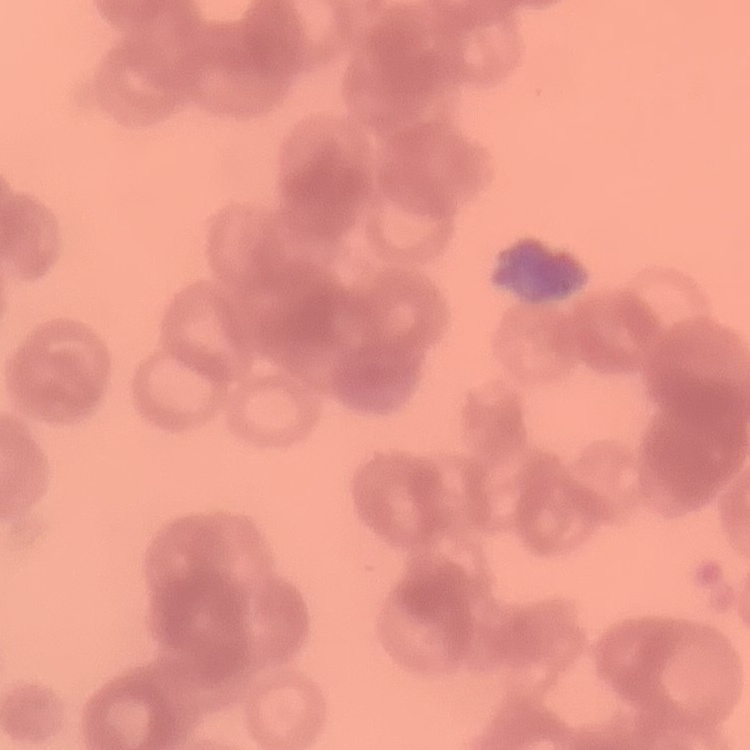
Summary:
  - Erythrocyte morphology: rouleaux formation
  - Stain: Field's or Giemsa
  - Preparation: thin blood film
  - Image type: square crop of a larger photomicrograph